Describe the morphology of the red blood cells.
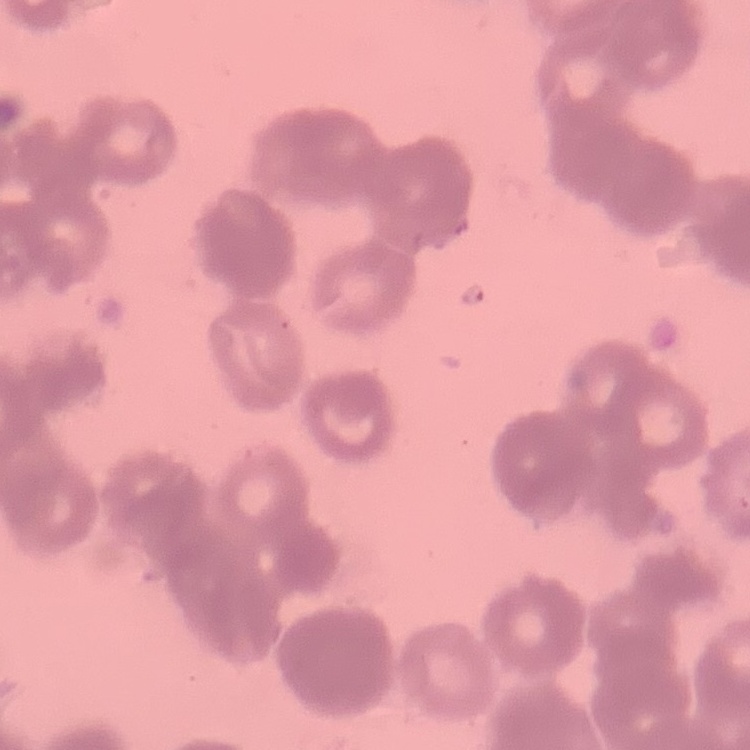

They show rouleaux formation.

Thin blood smear. One tile cut from a larger photomicrograph. Stained with either Field's or Giemsa.